Assess this cell for malaria.
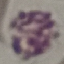
It is uninfected.

Summary:
  - Image type: cell patch, automatically extracted from a larger field of view and resized to 64 × 64 pixels
  - Capture: smartphone through the microscope eyepiece
  - Preparation: thin blood film
  - Stain: Giemsa